Report the malaria status of this cell.
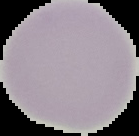
Uninfected.

{
  "image_type": "segmented cell region with the area outside set to black",
  "image_size": "139×136 pixels",
  "preparation": "thin blood smear"
}